Comment on the morphology of the red blood cells.
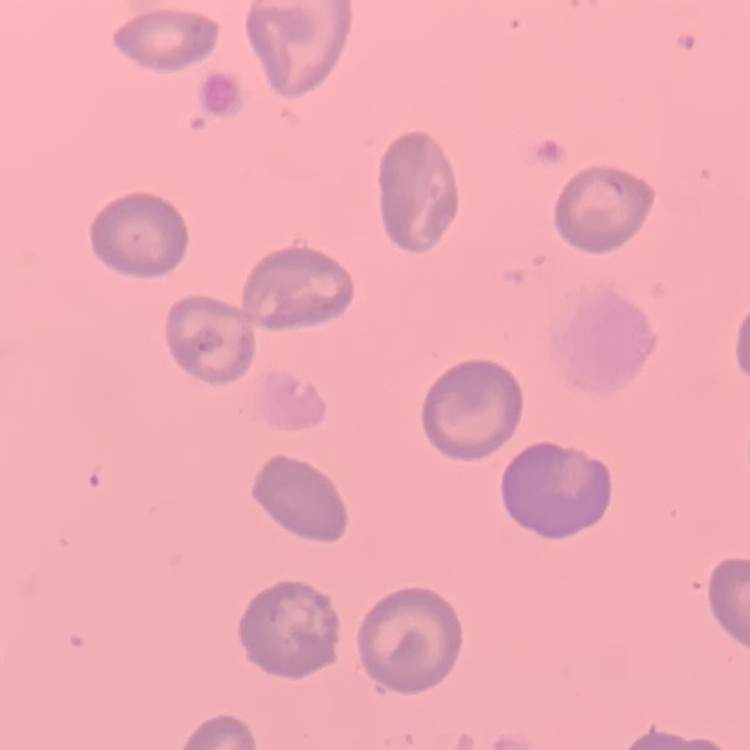

No rouleaux formation.

Summary:
  - Image type: square crop of a larger photomicrograph
  - Stain: Field's or Giemsa
  - Preparation: thin blood film